Assess this cell for malaria.
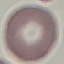

Uninfected.

image type = automatically extracted cell patch, resized to 64 × 64 pixels
stain = Giemsa
capture = smartphone through the microscope eyepiece
preparation = thin smear